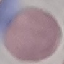

malaria status = uninfected
capture = smartphone through the microscope eyepiece
stain = Giemsa
image type = automatically extracted cell patch, resized to 64 × 64 pixels
preparation = thin smear